State the preparation type.
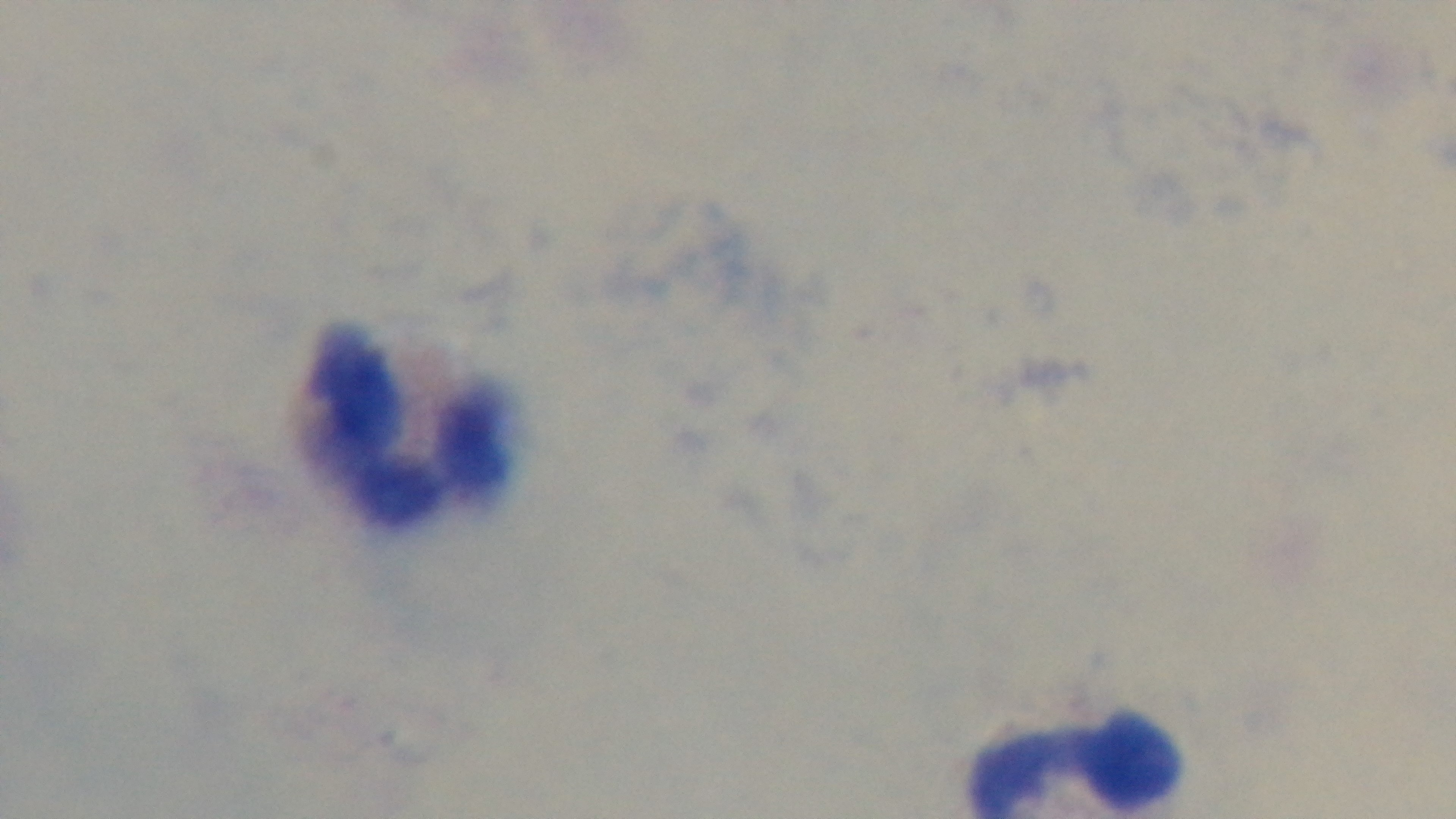

A thick smear.

Summary:
  - Stain: Giemsa
  - Modality: light microscopy
  - Malaria status: uninfected
  - Capture: mounted 4K digital camera
  - Field of view: single
  - Objective: 100x oil immersion